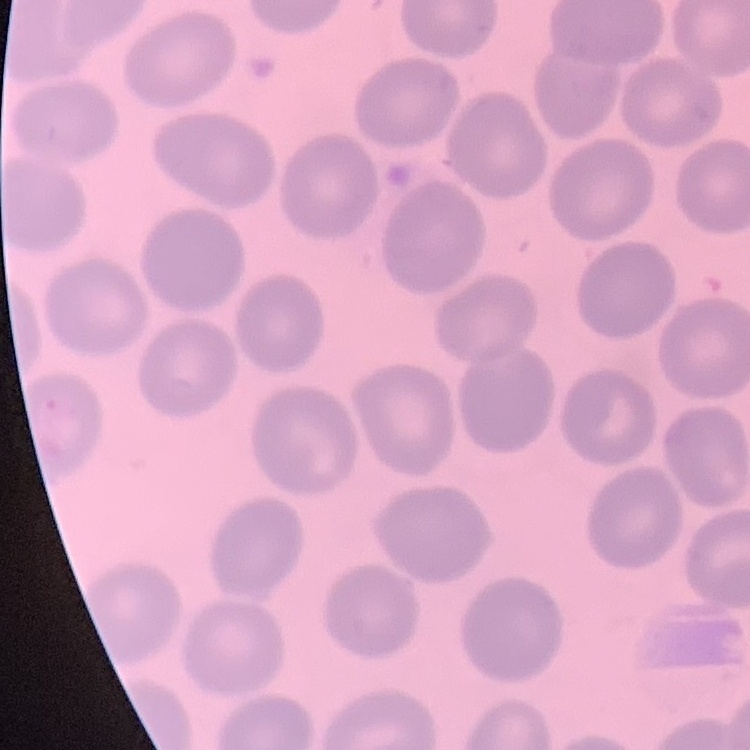

erythrocyte morphology = no rouleaux formation
preparation = thin blood smear
image type = one tile cut from a larger photomicrograph
stain = Field's or Giemsa